Assess the morphology of the erythrocytes.
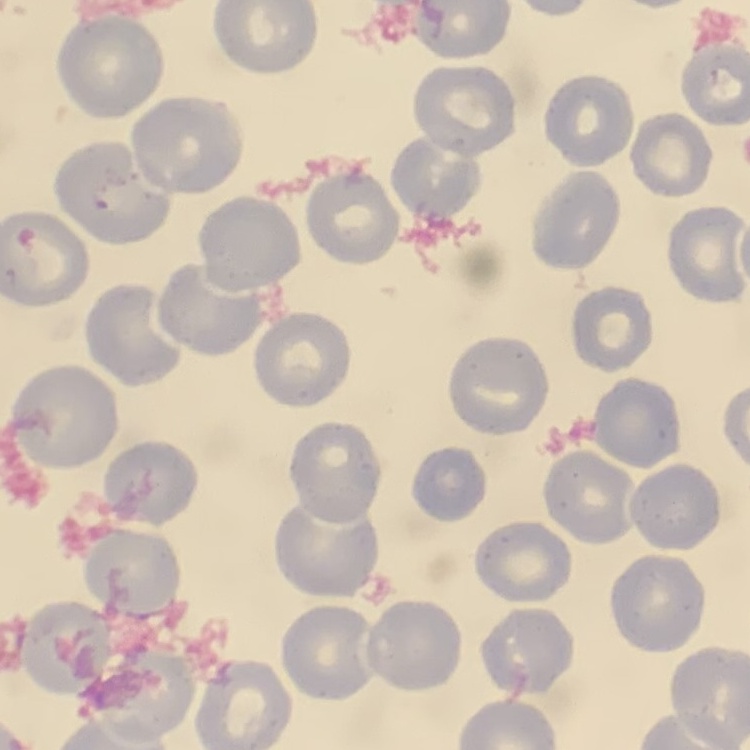
They show no rouleaux formation.

Summary:
  - Image type: one tile cut from a larger photomicrograph
  - Stain: Field's or Giemsa
  - Preparation: thin peripheral smear